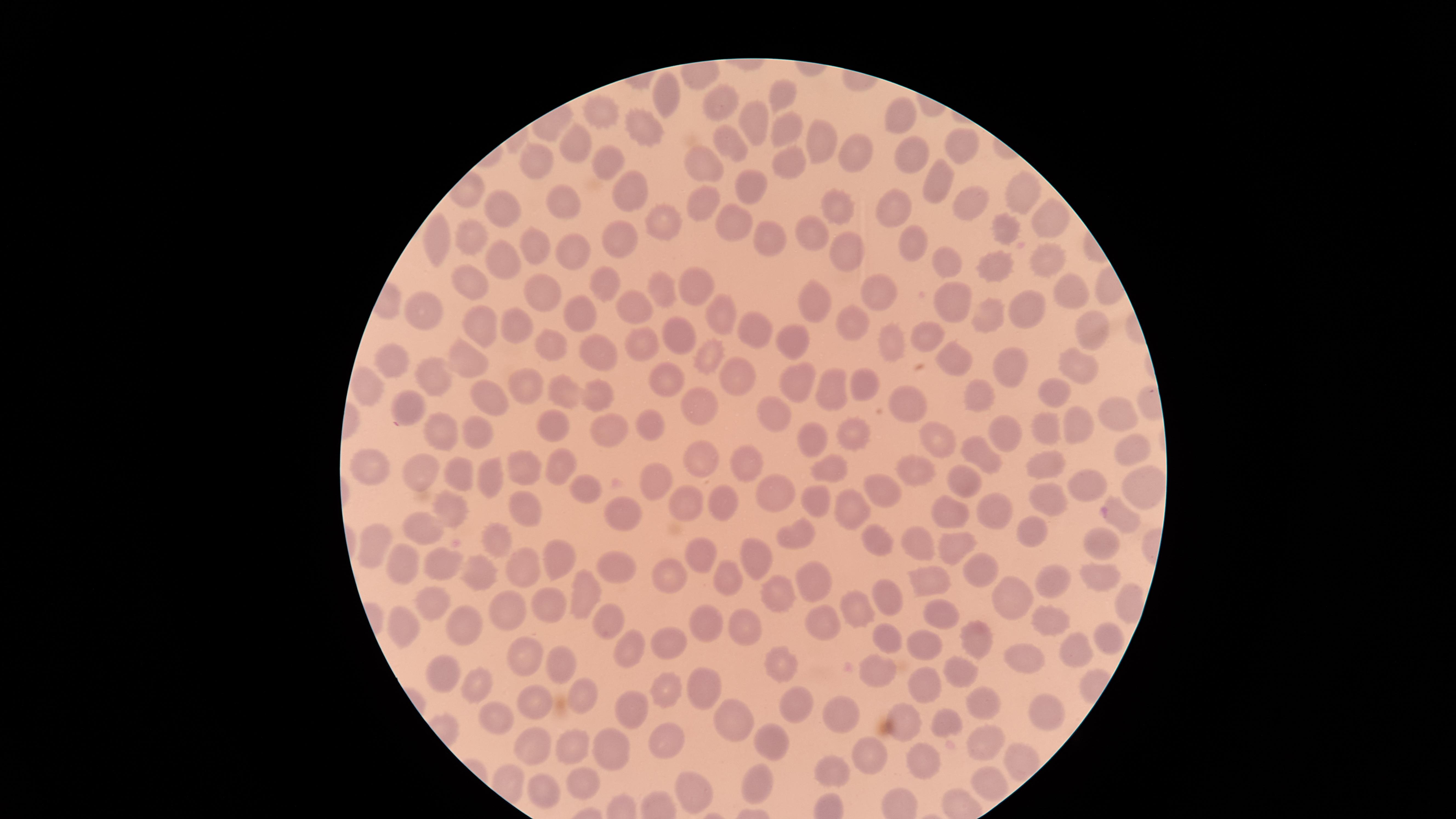
Approximate marker points as [x, y] in pixels. Uninfected red blood cells: [781, 97], [662, 98], [716, 101], [603, 110], [754, 115], [903, 115], [639, 129], [780, 130], [822, 138], [731, 141], [568, 148], [964, 149], [853, 151], [603, 159], [536, 163], [702, 163], [913, 165], [789, 170], [936, 175], [752, 179], [623, 186], [1024, 189], [701, 199], [566, 202], [966, 202], [839, 207], [887, 209], [499, 210], [1055, 218], [664, 219], [739, 220], [1002, 234], [470, 235], [808, 235], [763, 238], [439, 240], [910, 241], [619, 244], [534, 247], [845, 250], [573, 252], [497, 256], [946, 260], [994, 262], [1044, 262], [467, 281], [608, 283], [693, 287], [1062, 287], [669, 290], [883, 290], [541, 292], [954, 302], [813, 303], [629, 305], [1022, 309], [582, 311], [994, 313], [426, 314], [722, 317], [474, 320], [855, 321], [750, 326], [521, 328], [930, 335], [673, 336], [1096, 338], [896, 340], [795, 344], [546, 345], [645, 348], [596, 350], [465, 356], [390, 357], [708, 361], [960, 363], [1011, 365], [1078, 369], [743, 380], [858, 380], [435, 381], [670, 384], [800, 384], [526, 385], [369, 386], [596, 387], [832, 388], [1054, 388], [562, 390], [487, 392], [985, 395], [412, 398], [910, 400], [774, 410], [697, 411], [1120, 412], [650, 420], [1076, 420], [555, 421], [1047, 427], [439, 428], [607, 430], [472, 432], [849, 432], [1009, 436], [810, 437], [934, 438], [1128, 441], [702, 454], [981, 455], [1042, 463], [563, 464], [749, 465], [826, 466], [374, 468], [526, 470], [458, 472], [424, 473], [488, 473], [915, 473], [662, 479], [969, 480], [1089, 482], [1141, 485], [886, 488], [585, 489], [770, 491], [690, 499], [1044, 500], [527, 502], [722, 502], [813, 502], [456, 505], [990, 507], [856, 509], [950, 511], [626, 512], [1123, 519], [424, 525], [1033, 528], [800, 532], [875, 537], [504, 539], [955, 542], [920, 543], [1105, 544], [374, 547], [703, 554], [758, 557], [525, 561], [557, 561], [445, 562], [403, 565], [617, 566], [977, 566], [480, 569], [1052, 574], [674, 575], [727, 577], [1098, 578], [934, 579], [818, 583], [585, 590], [885, 592], [777, 595], [1012, 596], [1127, 598], [433, 600], [550, 600], [510, 605], [851, 608], [939, 609], [1053, 618], [736, 619], [826, 619], [604, 620], [710, 621], [403, 625], [457, 625], [1112, 639], [969, 640], [890, 642], [675, 645], [924, 647], [632, 648], [1074, 652], [522, 659], [558, 659], [1029, 661], [784, 664], [880, 671], [957, 671], [450, 675], [479, 684], [924, 687], [699, 689], [671, 692], [579, 693], [533, 700], [982, 700], [791, 705], [1048, 705], [841, 711], [629, 713], [493, 714], [906, 714], [731, 719], [666, 737], [985, 742], [537, 743], [567, 749], [614, 749], [777, 749], [872, 756], [1016, 758], [921, 763], [835, 766], [586, 784], [760, 786], [542, 787], [983, 787], [695, 788]. Thin smear of blood. Giemsa stain. The visible region is circular. Presence: no malaria parasites identified. One field of view of the specimen. Photographed with a smartphone camera through the microscope eyepiece. Image is 1456×819 pixels.